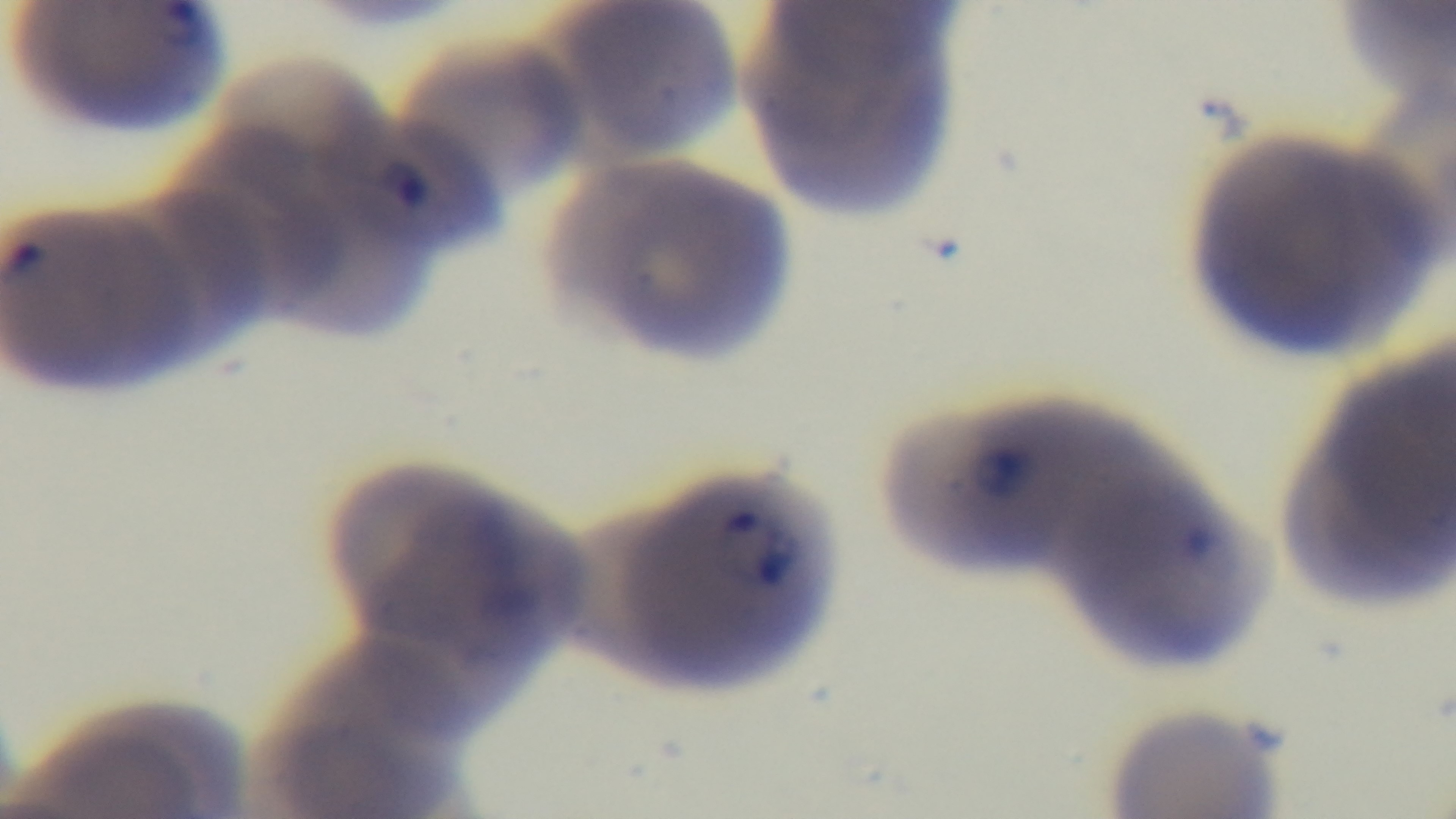
Summary:
  - Malaria status: positive
  - Field of view: one from the slide
  - Modality: light microscopy
  - Stain: Giemsa
  - Preparation: thin blood film
  - Objective: 100x oil immersion
  - Capture: mounted 4K digital camera